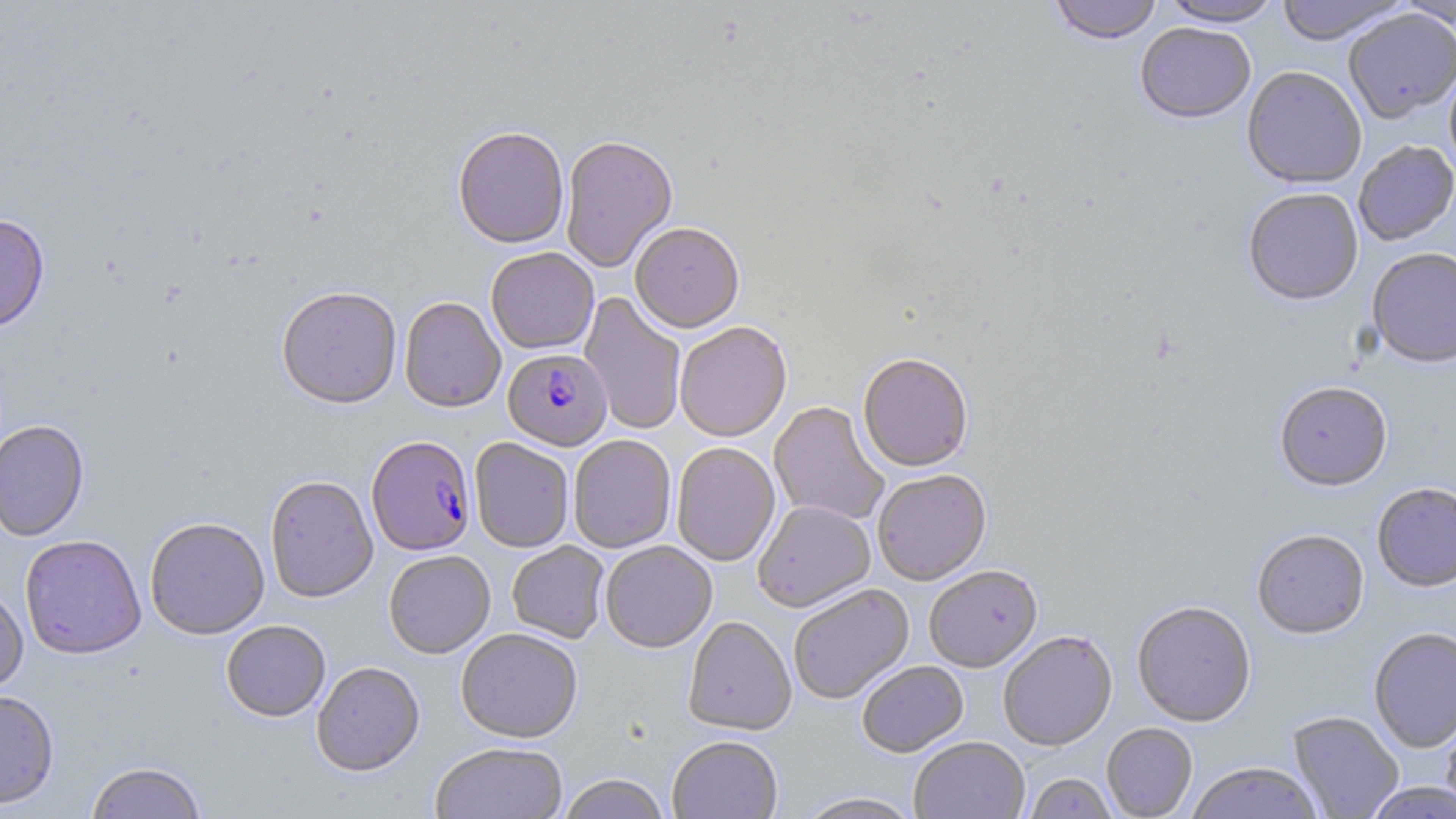
Summary:
  - Coordinate format: approximate bounding boxes as [x1, y1, x2, y2] in pixels
  - Plasmodium falciparum-infected red blood cell locations: [503, 349, 612, 451], [367, 437, 476, 557]
  - Uninfected red blood cell locations: [1048, 0, 1163, 46], [1159, 0, 1283, 28], [1273, 0, 1411, 46], [1394, 0, 1456, 29], [1343, 9, 1456, 124], [1135, 24, 1256, 126], [1443, 63, 1456, 182], [1242, 67, 1367, 190], [453, 129, 569, 251], [560, 138, 678, 273], [1354, 141, 1456, 246], [1243, 190, 1363, 307], [0, 214, 50, 334], [629, 224, 745, 335], [1366, 248, 1456, 370], [485, 249, 599, 356], [276, 288, 402, 411], [579, 292, 687, 436], [399, 298, 506, 414], [675, 323, 792, 443], [857, 356, 973, 473], [1274, 383, 1393, 493], [769, 402, 890, 525], [0, 420, 90, 543], [569, 435, 676, 553], [469, 439, 573, 553], [671, 443, 780, 567], [873, 471, 992, 586], [264, 476, 378, 604], [1372, 483, 1456, 594], [753, 501, 876, 614], [145, 518, 270, 640], [1251, 530, 1369, 641], [19, 535, 146, 661], [506, 542, 610, 643], [601, 542, 717, 653], [384, 551, 495, 659], [924, 567, 1042, 673], [788, 584, 914, 704], [0, 585, 29, 695], [1132, 602, 1255, 728], [683, 617, 796, 736], [221, 621, 331, 723], [1368, 627, 1456, 753], [456, 630, 583, 744], [997, 632, 1118, 751], [857, 662, 969, 758], [312, 663, 425, 778], [0, 690, 60, 811], [1287, 711, 1404, 819], [1440, 713, 1456, 817], [1102, 723, 1198, 818], [667, 737, 783, 819], [909, 737, 1030, 819], [430, 743, 568, 819], [85, 762, 207, 819], [1187, 763, 1323, 819], [1023, 773, 1119, 819], [558, 775, 672, 819], [1363, 782, 1456, 819], [795, 793, 922, 819]
  - Slide-level diagnosis: Plasmodium falciparum
  - Image size: 1456×819 pixels
  - Magnification: 1000x
  - Field of view: single
  - Stain: May-Grünwald-Giemsa
  - Preparation: thin blood smear
  - Modality: light microscopy